Identify the parasite.
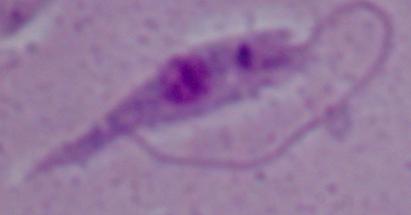

Leishmania.

Summary:
  - Modality: micrograph
  - Magnification: 1000x